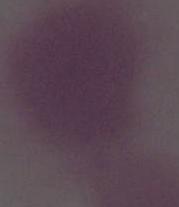

magnification = 1000x
identification = erythrocyte
modality = photomicrograph